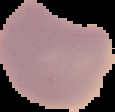 Result: negative for Plasmodium parasites. Segmented cell region on a black background. Image is 115×112 pixels. From a thin blood film.